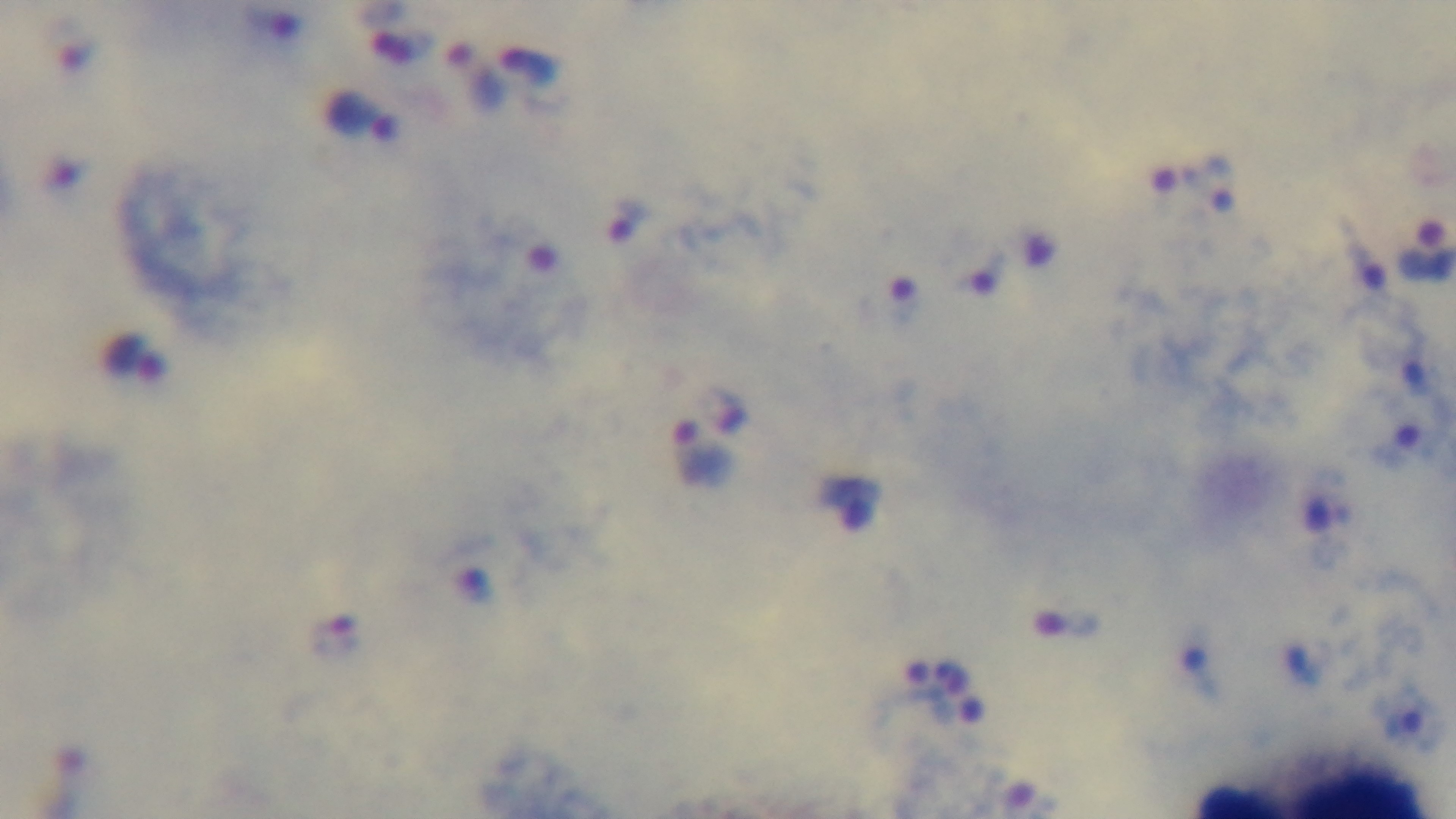
Summary:
  - Modality: light microscopy
  - Objective: 100x oil immersion
  - Field of view: one from the slide
  - Malaria status: positive
  - Stain: Giemsa
  - Capture: mounted 4K digital camera
  - Preparation: thick blood film